Name the parasite shown.
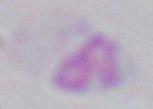
Toxoplasma gondii.

Summary:
  - Magnification: 1000x
  - Modality: photomicrograph